Give the extent of all uninfected red blood cells.
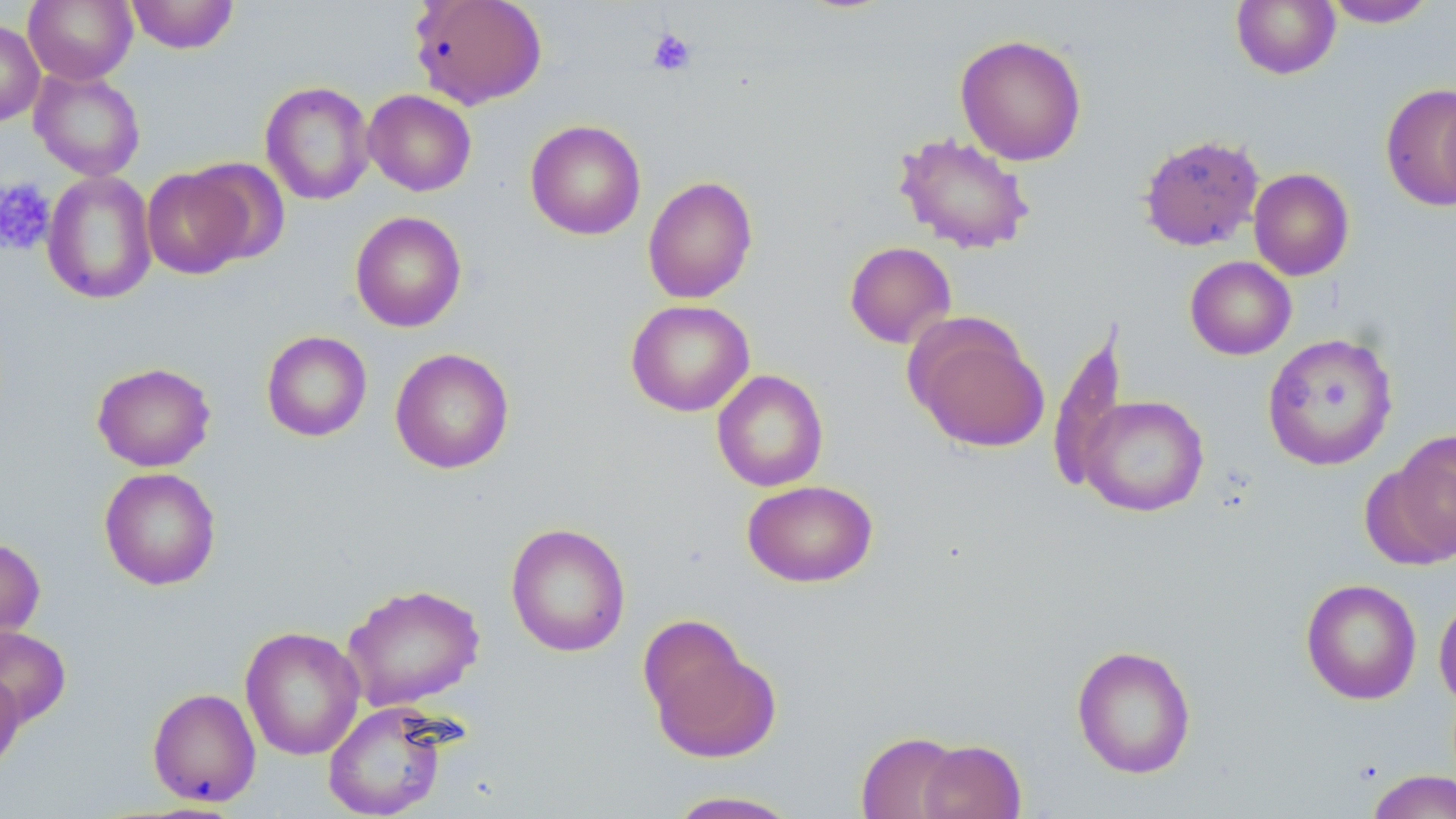
Approximate bounding boxes as (x1, y1, x2, y2) in pixels.
Uninfected red blood cells: (24, 0, 137, 85), (125, 0, 239, 53), (409, 0, 547, 110), (1231, 0, 1340, 79), (1321, 1, 1439, 28), (0, 19, 45, 127), (955, 33, 1087, 166), (29, 68, 146, 181), (260, 80, 375, 206), (1381, 83, 1456, 210), (1438, 87, 1456, 209), (363, 89, 477, 196), (525, 120, 646, 240), (893, 132, 1036, 254), (1138, 133, 1264, 252), (184, 158, 290, 267), (141, 167, 254, 279), (1248, 168, 1355, 280), (41, 171, 157, 305), (642, 175, 759, 304), (350, 211, 467, 333), (844, 241, 957, 348), (1185, 256, 1296, 360), (626, 299, 754, 417), (906, 315, 1049, 453), (261, 330, 372, 442), (1261, 332, 1398, 471), (390, 347, 514, 474), (91, 361, 216, 471), (712, 369, 829, 492), (1077, 394, 1210, 517), (1384, 429, 1456, 562), (98, 467, 221, 590), (742, 479, 878, 587), (505, 522, 631, 658), (0, 536, 46, 644), (1300, 578, 1422, 705), (341, 583, 485, 711), (1433, 591, 1456, 710), (0, 625, 72, 727), (240, 626, 365, 761), (645, 633, 780, 763), (1071, 644, 1197, 779), (0, 669, 26, 777), (147, 687, 262, 806), (323, 701, 452, 818), (857, 731, 965, 818), (917, 739, 1026, 819), (1365, 770, 1456, 819), (662, 790, 804, 818).

{
  "slide_level_diagnosis": "negative for blood parasites",
  "platelet_locations": "approximate bounding boxes as (x1, y1, x2, y2) in pixels: (647, 28, 697, 76), (0, 178, 56, 256)",
  "image_size": "1456×819 pixels",
  "preparation": "thin blood smear",
  "field_of_view": "single",
  "modality": "light microscopy",
  "stain": "May-Grünwald-Giemsa",
  "magnification": "1000x"
}